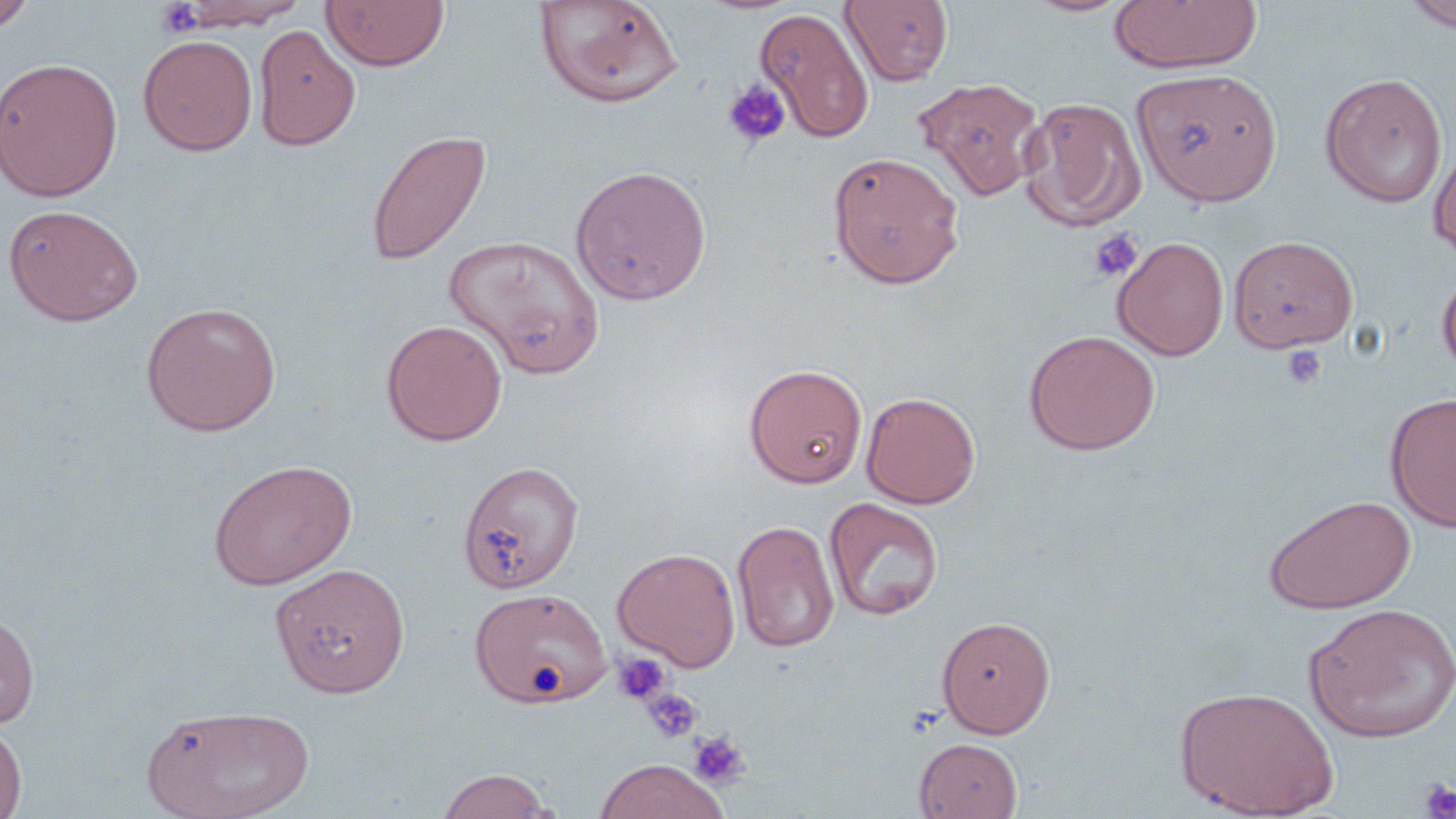

Summary:
  - Coordinate format: approximate bounding boxes as named x1/y1/x2/y2 corners in pixels
  - Platelet locations: (x1=155, y1=1, x2=207, y2=38), (x1=722, y1=78, x2=791, y2=148), (x1=1088, y1=229, x2=1143, y2=282), (x1=1282, y1=345, x2=1327, y2=389), (x1=612, y1=653, x2=673, y2=705), (x1=642, y1=687, x2=703, y2=743), (x1=688, y1=730, x2=750, y2=789), (x1=1420, y1=779, x2=1456, y2=819)
  - Uninfected red blood cell locations: (x1=0, y1=0, x2=38, y2=34), (x1=321, y1=0, x2=449, y2=72), (x1=841, y1=0, x2=953, y2=86), (x1=1403, y1=0, x2=1456, y2=32), (x1=165, y1=1, x2=312, y2=32), (x1=533, y1=1, x2=684, y2=108), (x1=1108, y1=1, x2=1263, y2=73), (x1=756, y1=6, x2=873, y2=143), (x1=253, y1=23, x2=360, y2=151), (x1=138, y1=33, x2=258, y2=156), (x1=0, y1=57, x2=123, y2=202), (x1=1132, y1=67, x2=1283, y2=206), (x1=1319, y1=73, x2=1447, y2=208), (x1=914, y1=78, x2=1047, y2=201), (x1=1020, y1=97, x2=1144, y2=232), (x1=365, y1=129, x2=491, y2=266), (x1=1429, y1=141, x2=1456, y2=260), (x1=827, y1=151, x2=965, y2=289), (x1=570, y1=165, x2=712, y2=305), (x1=3, y1=204, x2=144, y2=327), (x1=444, y1=234, x2=606, y2=378), (x1=1228, y1=235, x2=1358, y2=352), (x1=1113, y1=236, x2=1229, y2=360), (x1=1437, y1=268, x2=1456, y2=381), (x1=141, y1=301, x2=281, y2=436), (x1=381, y1=319, x2=507, y2=446), (x1=1023, y1=330, x2=1160, y2=455), (x1=744, y1=363, x2=868, y2=488), (x1=861, y1=391, x2=981, y2=508), (x1=1385, y1=393, x2=1456, y2=531), (x1=207, y1=458, x2=357, y2=590), (x1=458, y1=459, x2=584, y2=593), (x1=1263, y1=494, x2=1416, y2=614), (x1=824, y1=497, x2=944, y2=621), (x1=732, y1=520, x2=840, y2=653), (x1=612, y1=547, x2=741, y2=670), (x1=270, y1=563, x2=411, y2=697), (x1=471, y1=588, x2=610, y2=708), (x1=1304, y1=603, x2=1456, y2=742), (x1=0, y1=608, x2=40, y2=730), (x1=937, y1=615, x2=1055, y2=738), (x1=1175, y1=686, x2=1339, y2=818), (x1=142, y1=703, x2=313, y2=819), (x1=0, y1=722, x2=27, y2=819), (x1=914, y1=737, x2=1023, y2=819), (x1=594, y1=759, x2=727, y2=818), (x1=435, y1=768, x2=556, y2=818)
  - Slide-level diagnosis: no evidence of blood parasites
  - Image size: 1456×819 pixels
  - Preparation: thin blood smear
  - Stain: May-Grünwald-Giemsa
  - Field of view: single
  - Modality: optical microscopy
  - Magnification: 1000x